Identify the cell.
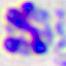
This is a leukocyte.

modality = photomicrograph
magnification = 400x